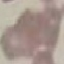

{
  "result": "no malaria parasites detected",
  "image_type": "cell patch, automatically extracted from a larger field of view and resized to 64 × 64 pixels",
  "capture": "smartphone through the microscope eyepiece",
  "stain": "Giemsa",
  "preparation": "thin blood film"
}